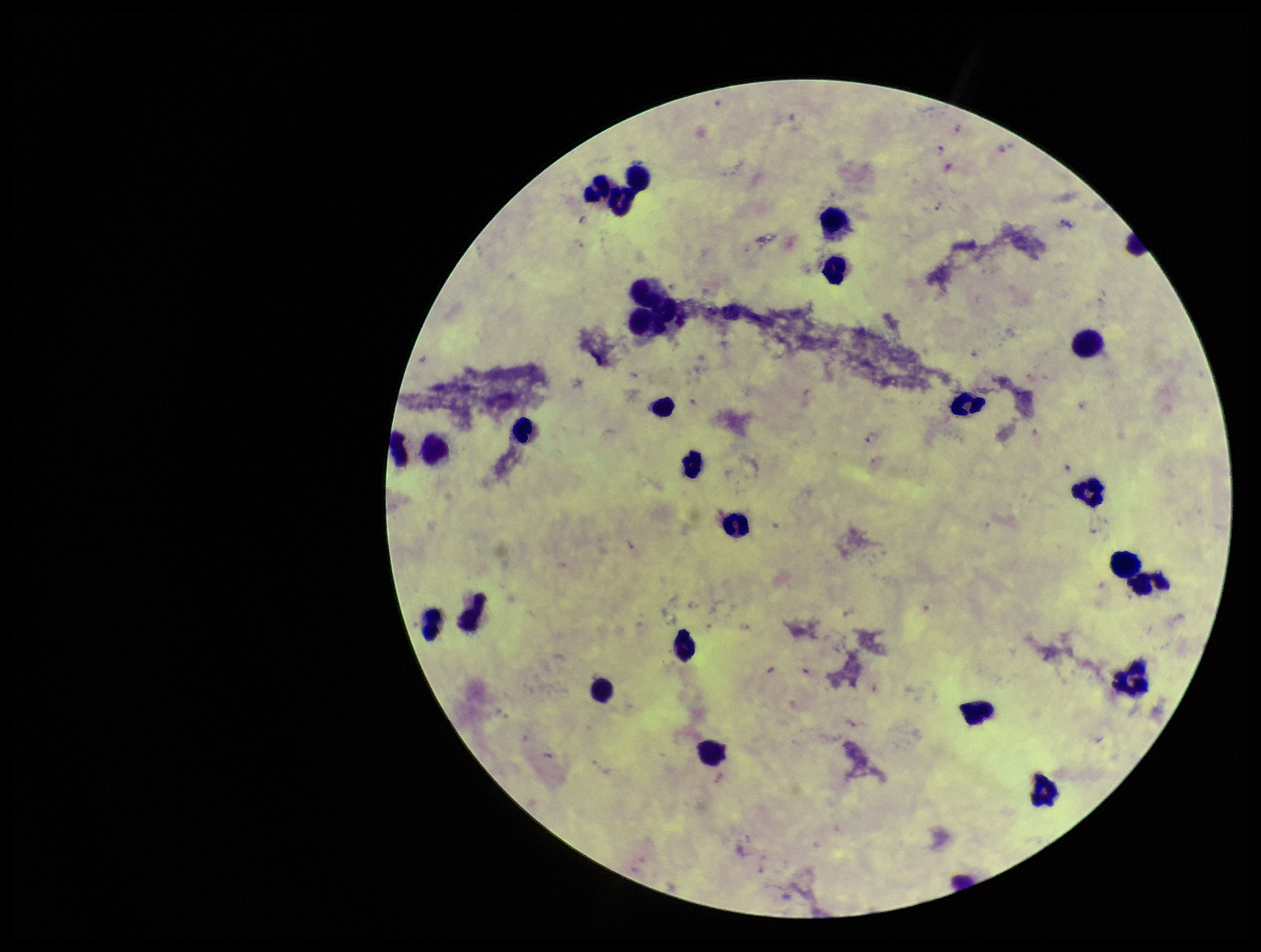

Summary:
  - Leukocyte count: 25
  - Image size: 1261×952 pixels
  - Patient malaria status: infected
  - Species reported for this patient: Plasmodium falciparum
  - Parasite count: 11
  - Capture: smartphone photograph through the microscope eyepiece
  - Plasmodium parasites: identified
  - Preparation: thick blood smear
  - Field of view: one from this slide
  - Stain: Giemsa